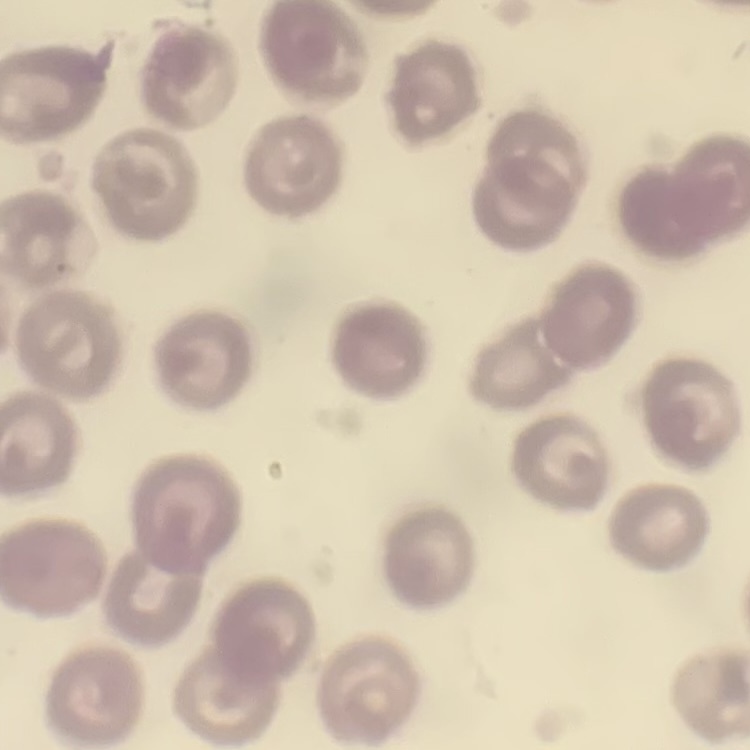

Summary:
  - Erythrocyte morphology: no rouleaux formation
  - Preparation: thin blood smear
  - Image type: one tile cut from a larger photomicrograph
  - Stain: Field's or Giemsa